Assess for Plasmodium parasites.
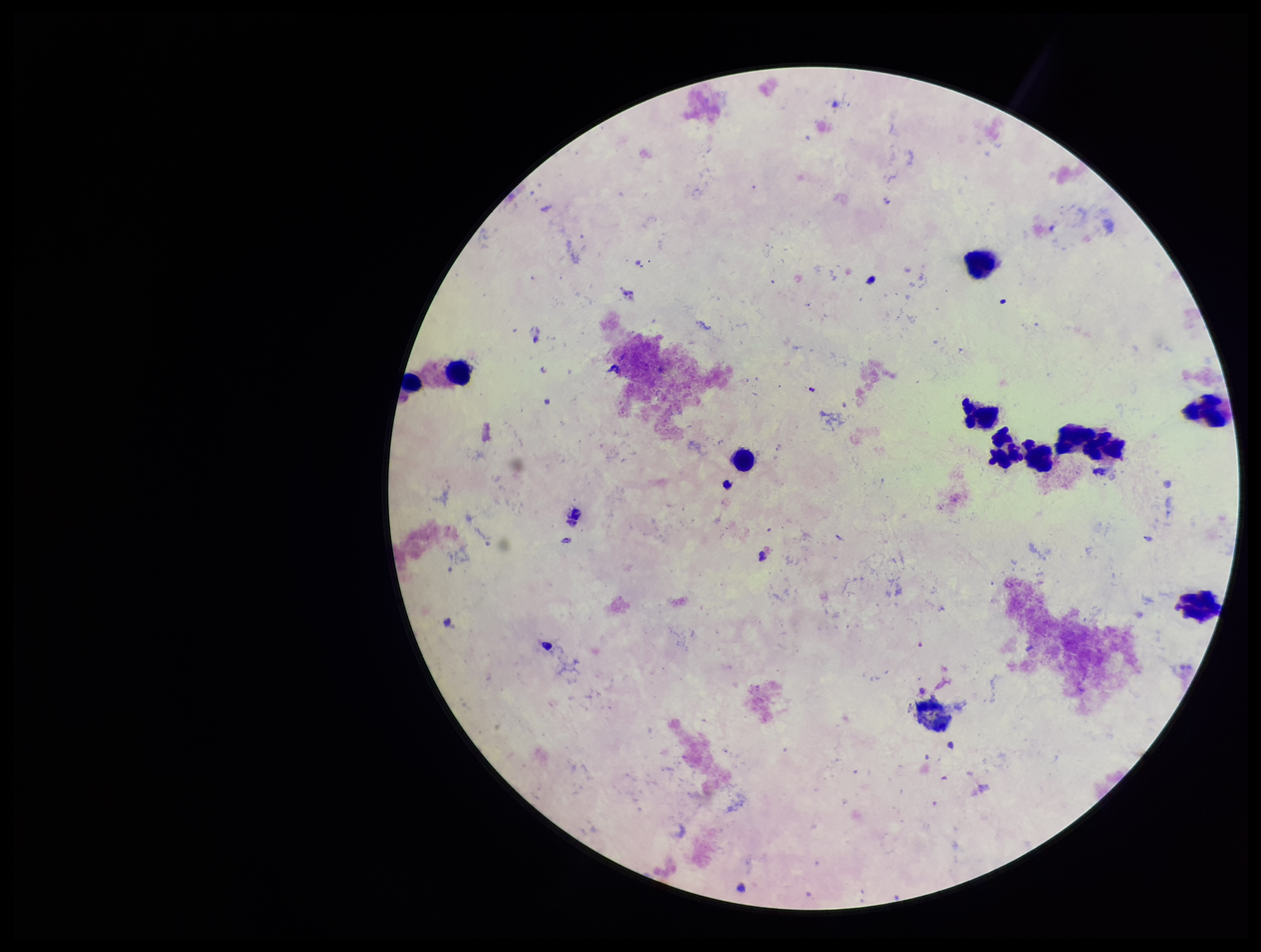
None identified.

capture = smartphone photograph through the microscope eyepiece
stain = Giemsa
preparation = thick blood smear
patient malaria status = negative
image size = 1261×952 pixels
leukocyte count = 10
field of view = one from this slide
parasite count = 0